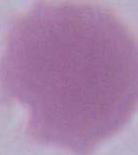

identification = erythrocyte
magnification = 1000x
modality = micrograph